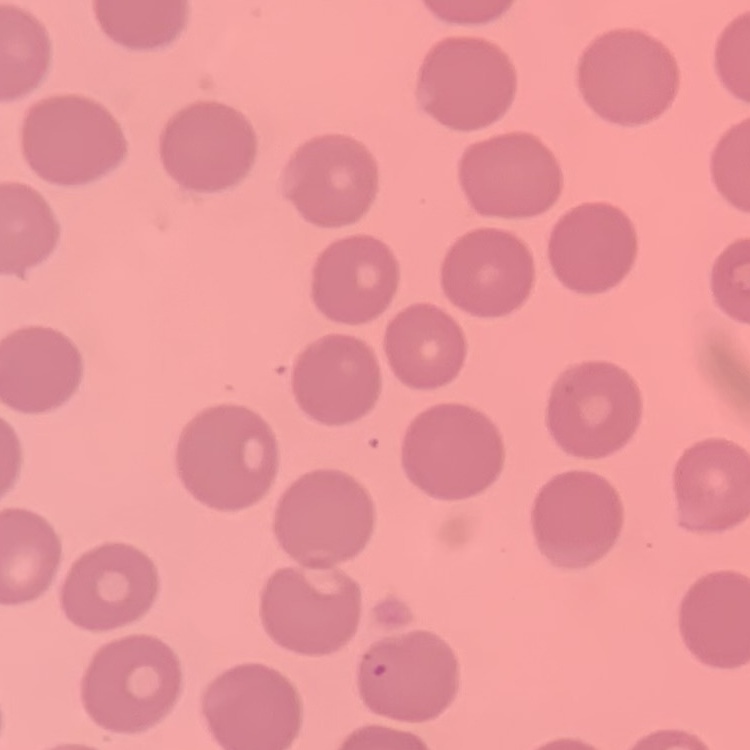

The erythrocytes exhibit no rouleaux formation. Thin blood smear. Square crop of a larger photomicrograph. Stained with either Field's or Giemsa.